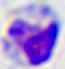
modality: micrograph
identification: leukocyte
magnification: 400x